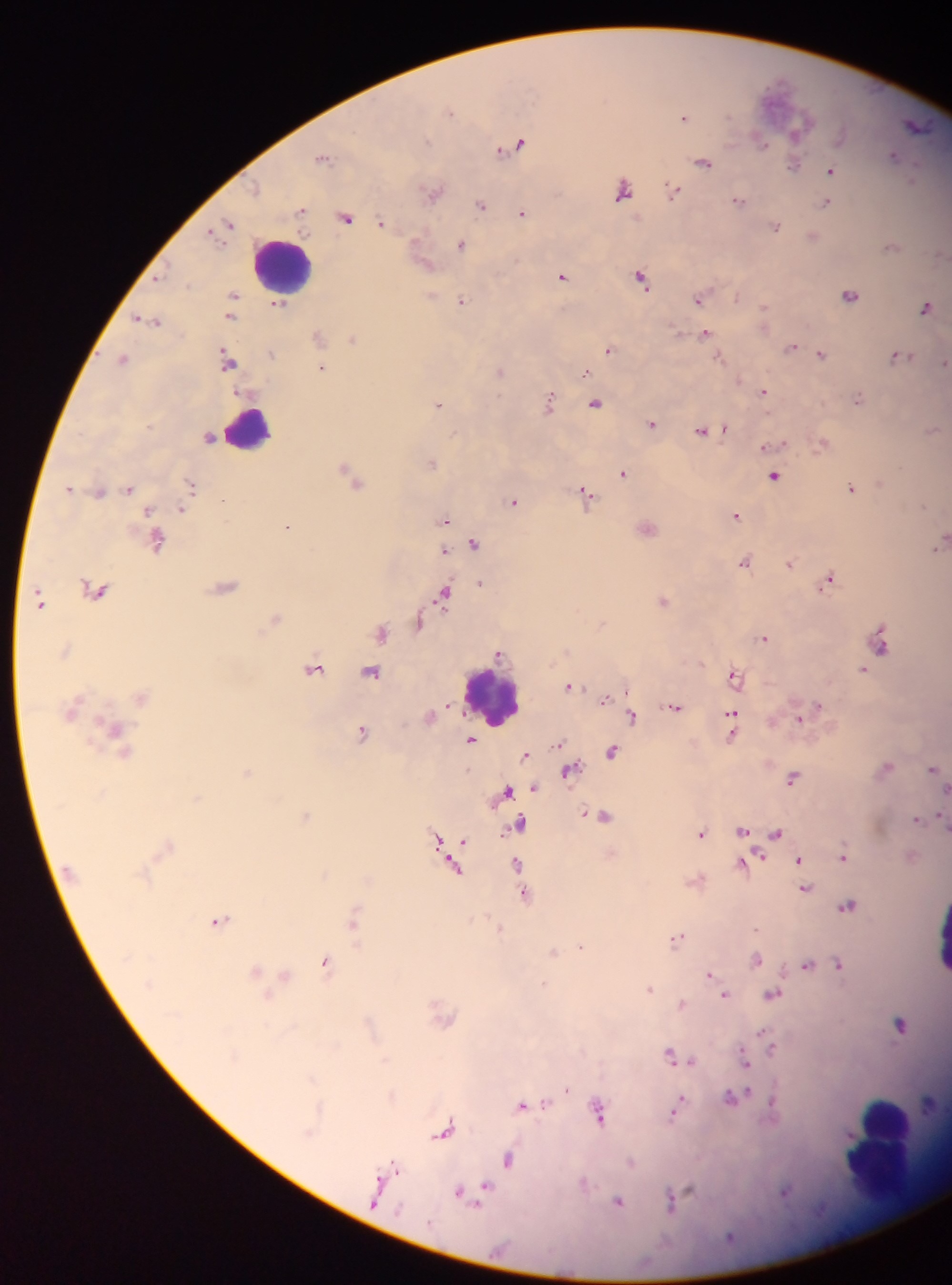
country = Ghana
field of view = single
image size = 952×1285 pixels
malaria parasite locations = approximate centers as (x, y) in pixels: (776, 91), (451, 112), (685, 117), (800, 124), (915, 125), (760, 142), (516, 145), (893, 156), (324, 157), (703, 162), (793, 165), (830, 171), (622, 189), (673, 192), (433, 193), (739, 200), (826, 203), (482, 205), (302, 211), (522, 213), (346, 218), (383, 223), (229, 224), (775, 227), (813, 237), (461, 244), (891, 246), (422, 259), (562, 276), (641, 278), (850, 295), (234, 296), (433, 297), (699, 298), (463, 301), (279, 305), (925, 307), (764, 312), (230, 317), (149, 318), (706, 334), (319, 337), (353, 339), (791, 347), (610, 350), (273, 353), (820, 353), (897, 357), (124, 358), (719, 358), (228, 361), (944, 363), (322, 368), (500, 371), (584, 372), (764, 391), (859, 398), (549, 403), (438, 404), (595, 404), (652, 424), (724, 429), (932, 430), (701, 431), (210, 437), (822, 442), (432, 463), (623, 474), (774, 477), (354, 480), (192, 485), (70, 488), (129, 488), (851, 488), (100, 492), (586, 497), (514, 502), (183, 509), (150, 510), (736, 515), (444, 520), (288, 527), (647, 529), (158, 542), (940, 542), (475, 544), (445, 551), (745, 560), (790, 564), (828, 580), (481, 584), (226, 587), (97, 589), (444, 593), (663, 600), (41, 601), (275, 618), (420, 622), (381, 633), (764, 638), (882, 645), (499, 653), (314, 669), (862, 670), (372, 672), (734, 676), (571, 686), (605, 699), (674, 706), (817, 707), (632, 717), (800, 717), (732, 718), (116, 729), (362, 733), (471, 740), (559, 743), (612, 752), (525, 755), (885, 767), (932, 769), (570, 770), (247, 773), (793, 777), (533, 789), (507, 792), (306, 815), (604, 816), (917, 818), (519, 826), (742, 830), (701, 833), (776, 834), (436, 839), (463, 841), (168, 845), (844, 856), (799, 860), (517, 865), (743, 865), (455, 867), (805, 888), (525, 895), (848, 905), (220, 921), (353, 921), (499, 930), (677, 938), (581, 946), (553, 952), (756, 959), (325, 962), (838, 964), (806, 965), (257, 971), (709, 973), (285, 975), (650, 988), (772, 994), (724, 995), (682, 1004), (901, 1025), (764, 1035), (771, 1047), (669, 1054), (744, 1060), (691, 1061), (566, 1089), (733, 1096), (545, 1104), (773, 1104), (521, 1106), (677, 1107), (598, 1112), (444, 1132), (509, 1159), (393, 1167), (484, 1192), (785, 1192), (461, 1193), (683, 1194), (377, 1196), (671, 1200), (619, 1202)
preparation = thick blood smear
capture = mobile-phone photograph through a microscope
leukocyte locations = approximate centers as (x, y) in pixels: (284, 263), (252, 427), (494, 699), (887, 1145)